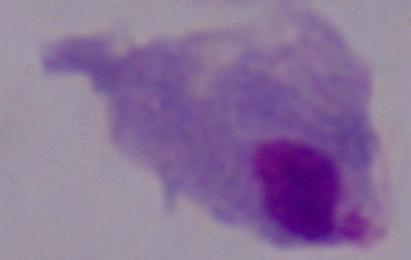
Summary:
  - Magnification: 1000x
  - Identification: trichomonad
  - Modality: micrograph